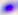
400x magnification. Photomicrograph. Toxoplasma gondii is seen.